Assess the morphology of the red blood cells.
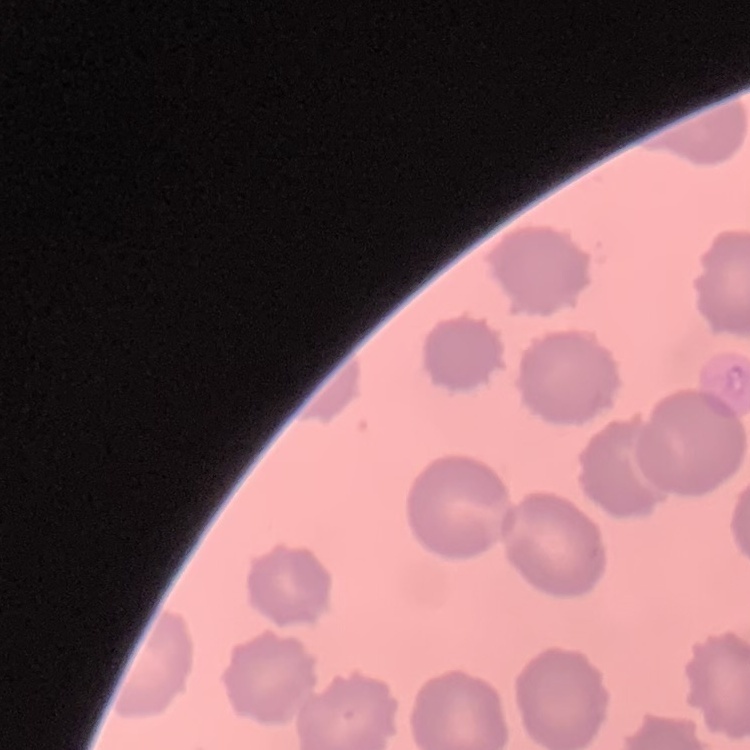
They show no rouleaux formation.

Summary:
  - Stain: Field's or Giemsa
  - Preparation: thin peripheral smear
  - Image type: square crop of a larger photomicrograph